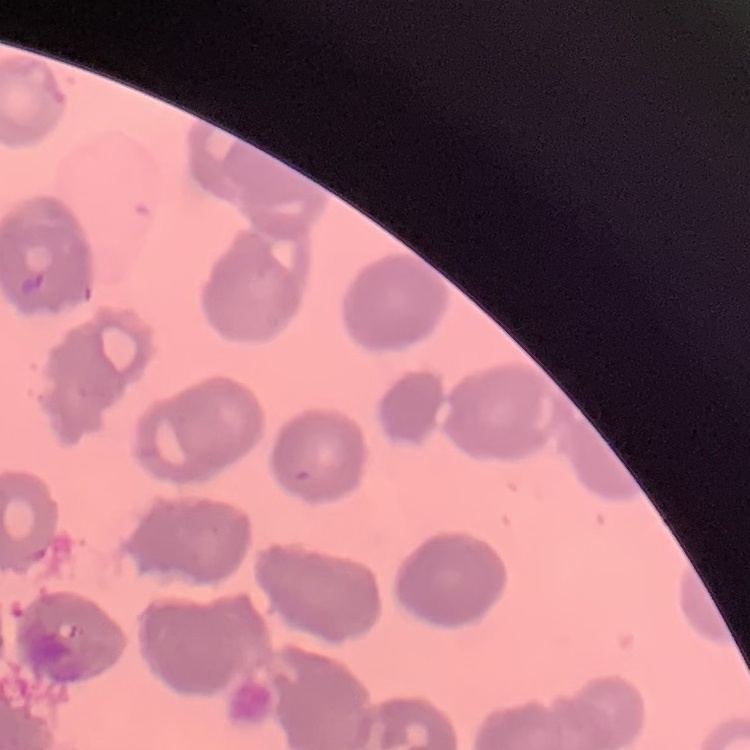 The erythrocytes exhibit rouleaux formation. Field's or Giemsa stain. Square crop of a larger photomicrograph. Thin peripheral smear.